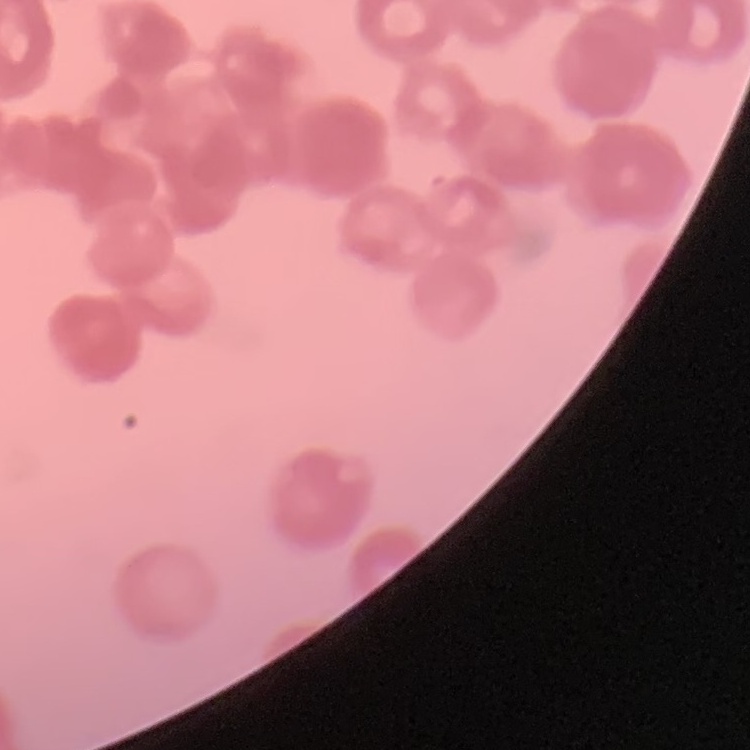

red_blood_cell_morphology: rouleaux formation
stain: Field's or Giemsa
image_type: one tile cut from a larger photomicrograph
preparation: thin blood smear